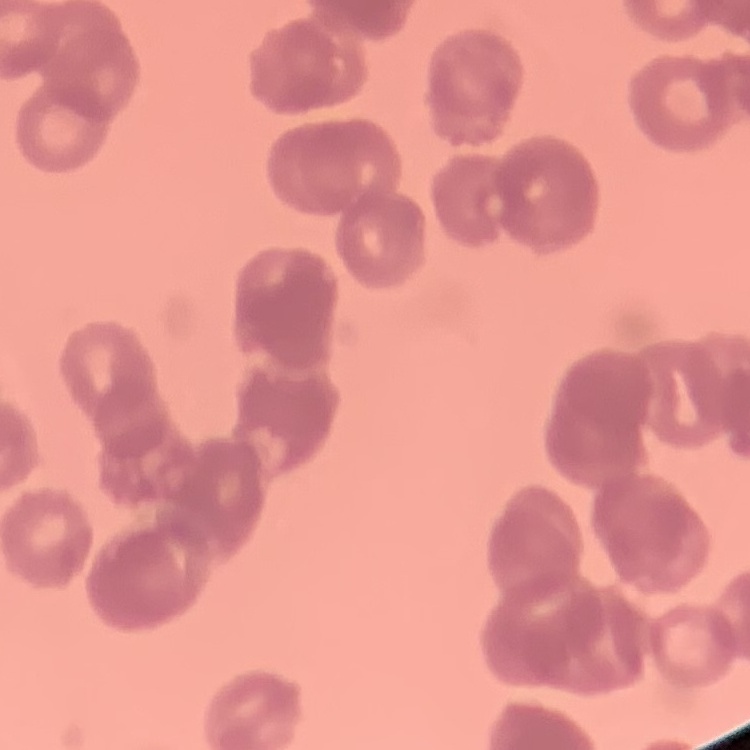
The red blood cells show rouleaux formation. Thin blood film. Stained with either Field's or Giemsa. One tile cut from a larger photomicrograph.